Give the extent of all Babesia divergens-infected red blood cells.
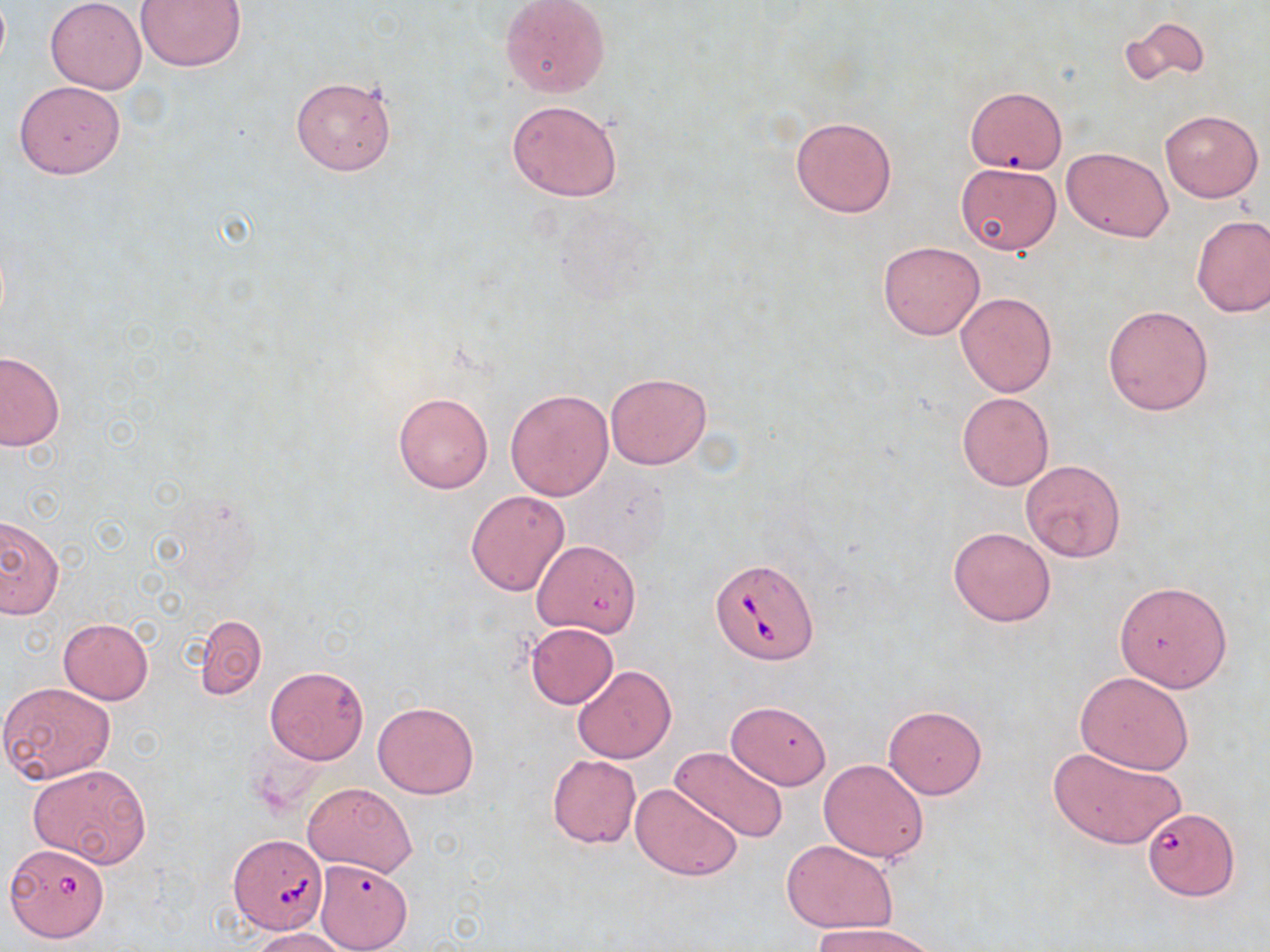
Approximate bounding boxes as [x1, y1, x2, y2] in pixels.
Babesia divergens-infected red blood cells: [710, 557, 818, 665], [1142, 807, 1238, 898], [229, 835, 327, 933], [10, 850, 107, 944].

Summary:
  - Uninfected red blood cell locations: [46, 0, 146, 93], [500, 0, 611, 100], [136, 1, 247, 72], [1120, 16, 1209, 90], [290, 75, 397, 176], [13, 80, 126, 180], [964, 87, 1066, 173], [506, 99, 624, 202], [1161, 110, 1263, 201], [790, 115, 898, 218], [1063, 146, 1173, 242], [956, 164, 1062, 255], [1191, 214, 1270, 317], [878, 240, 984, 340], [956, 292, 1057, 396], [1103, 303, 1214, 415], [0, 351, 64, 451], [606, 372, 711, 470], [505, 389, 614, 500], [392, 391, 493, 493], [957, 392, 1053, 491], [1020, 460, 1126, 562], [465, 490, 570, 596], [0, 514, 62, 618], [948, 526, 1056, 627], [1116, 580, 1232, 691], [193, 614, 267, 700], [58, 618, 154, 704], [524, 622, 620, 708], [573, 664, 676, 764], [265, 665, 368, 764], [1074, 672, 1195, 774], [0, 683, 115, 786], [727, 699, 830, 789], [374, 701, 478, 799], [883, 705, 987, 799], [1047, 743, 1187, 851], [673, 746, 789, 842], [547, 754, 641, 849], [819, 758, 929, 864], [28, 762, 151, 868], [302, 782, 417, 877], [631, 782, 744, 881], [781, 842, 897, 932], [314, 859, 412, 952], [811, 923, 940, 952], [249, 927, 352, 951]
  - Slide-level diagnosis: Babesia divergens
  - Image size: 1270×952 pixels
  - Magnification: 1000x
  - Field of view: one of a larger specimen
  - Modality: light microscopy
  - Preparation: thin blood smear
  - Stain: May-Grünwald-Giemsa